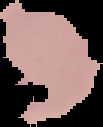

Cell region segmented out of the field of view; the surrounding area is masked to black. Image is 103×127 pixels. From a thin blood smear. Result: no Plasmodium parasites seen.